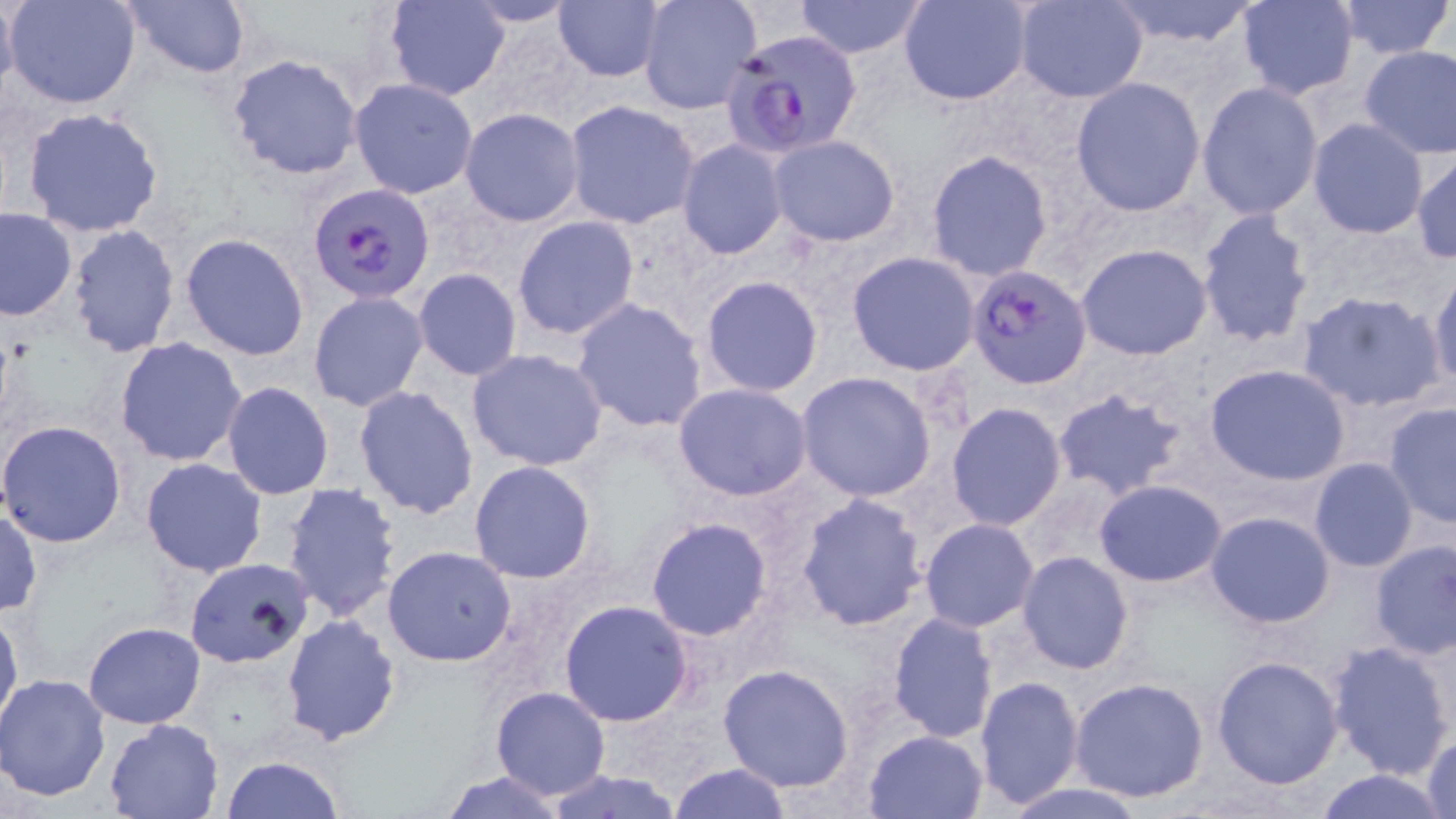 Approximate bounding boxes as (x1, y1, x2, y2) in pixels. Plasmodium falciparum-infected red blood cell locations: (724, 34, 868, 176), (308, 184, 436, 306), (966, 265, 1092, 389). Uninfected red blood cell locations: (0, 0, 18, 103), (5, 0, 140, 109), (122, 0, 251, 79), (385, 0, 510, 100), (637, 0, 761, 115), (794, 0, 928, 58), (900, 0, 1034, 105), (1013, 0, 1149, 102), (1108, 0, 1262, 49), (1235, 0, 1360, 101), (1334, 0, 1453, 59), (460, 1, 580, 27), (553, 2, 664, 81), (1358, 45, 1456, 161), (226, 53, 362, 180), (1070, 77, 1206, 216), (349, 78, 479, 199), (1196, 81, 1324, 220), (564, 100, 701, 229), (22, 106, 166, 238), (459, 108, 584, 227), (1307, 118, 1430, 238), (767, 135, 900, 246), (677, 139, 790, 260), (926, 151, 1052, 282), (1411, 151, 1456, 263), (0, 209, 76, 321), (1196, 209, 1315, 348), (512, 216, 639, 342), (67, 224, 179, 358), (180, 233, 309, 360), (1077, 243, 1213, 360), (846, 252, 981, 375), (413, 269, 523, 380), (1427, 270, 1456, 393), (699, 274, 825, 398), (1294, 288, 1448, 414), (308, 290, 429, 412), (571, 297, 710, 432), (114, 337, 248, 467), (466, 348, 608, 471), (1204, 363, 1351, 485), (796, 372, 937, 501), (221, 381, 334, 500), (672, 382, 813, 501), (353, 386, 479, 519), (1052, 386, 1190, 502), (1382, 401, 1456, 529), (945, 402, 1066, 531), (0, 420, 127, 547), (140, 457, 268, 577), (1308, 459, 1419, 572), (468, 461, 595, 584), (1094, 479, 1228, 588), (281, 482, 403, 622), (795, 492, 930, 631), (0, 511, 42, 616), (1206, 512, 1334, 628), (646, 518, 773, 641), (919, 519, 1039, 632), (1368, 540, 1455, 661), (382, 546, 517, 665), (1016, 551, 1134, 674), (183, 557, 313, 671), (559, 598, 695, 726), (0, 606, 22, 734), (887, 612, 999, 743), (280, 614, 401, 745), (83, 622, 206, 729), (1327, 639, 1455, 780), (1210, 655, 1344, 790), (719, 663, 857, 792), (0, 673, 111, 801), (974, 677, 1084, 808), (1069, 677, 1211, 803), (491, 686, 611, 800), (103, 718, 221, 818), (1420, 728, 1455, 819), (864, 729, 987, 817), (220, 757, 346, 817), (670, 763, 791, 818), (1314, 768, 1450, 819), (439, 770, 565, 817), (539, 771, 684, 819), (998, 782, 1154, 819). Slide-level diagnosis: Plasmodium falciparum. Captured at 1000x magnification. May-Grünwald-Giemsa stain. Thin blood film. Light microscopy. One field of a larger specimen. Image is 1456×819 pixels.